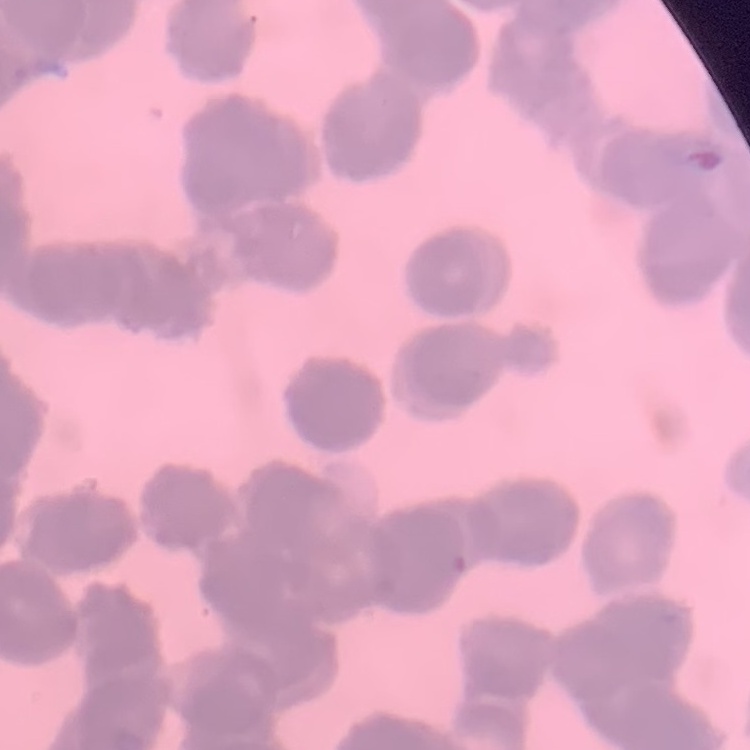

Summary:
  - Erythrocyte morphology: rouleaux formation
  - Image type: one tile cut from a larger photomicrograph
  - Preparation: thin peripheral smear
  - Stain: Field's or Giemsa